Assess the morphology of the red blood cells.
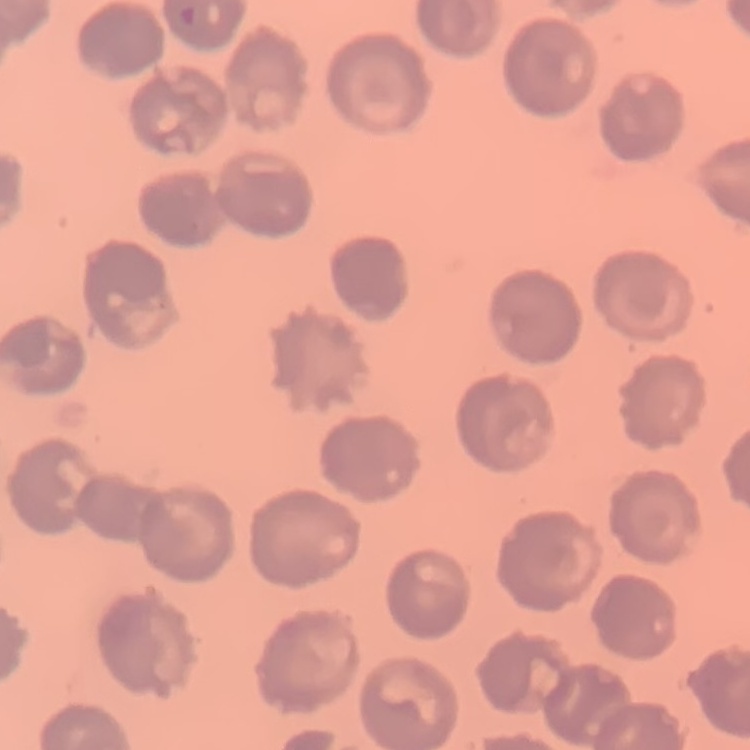
They show no rouleaux formation.

stain = Field's or Giemsa
preparation = thin peripheral smear
image type = square crop of a larger photomicrograph